Evaluate for Plasmodium parasites.
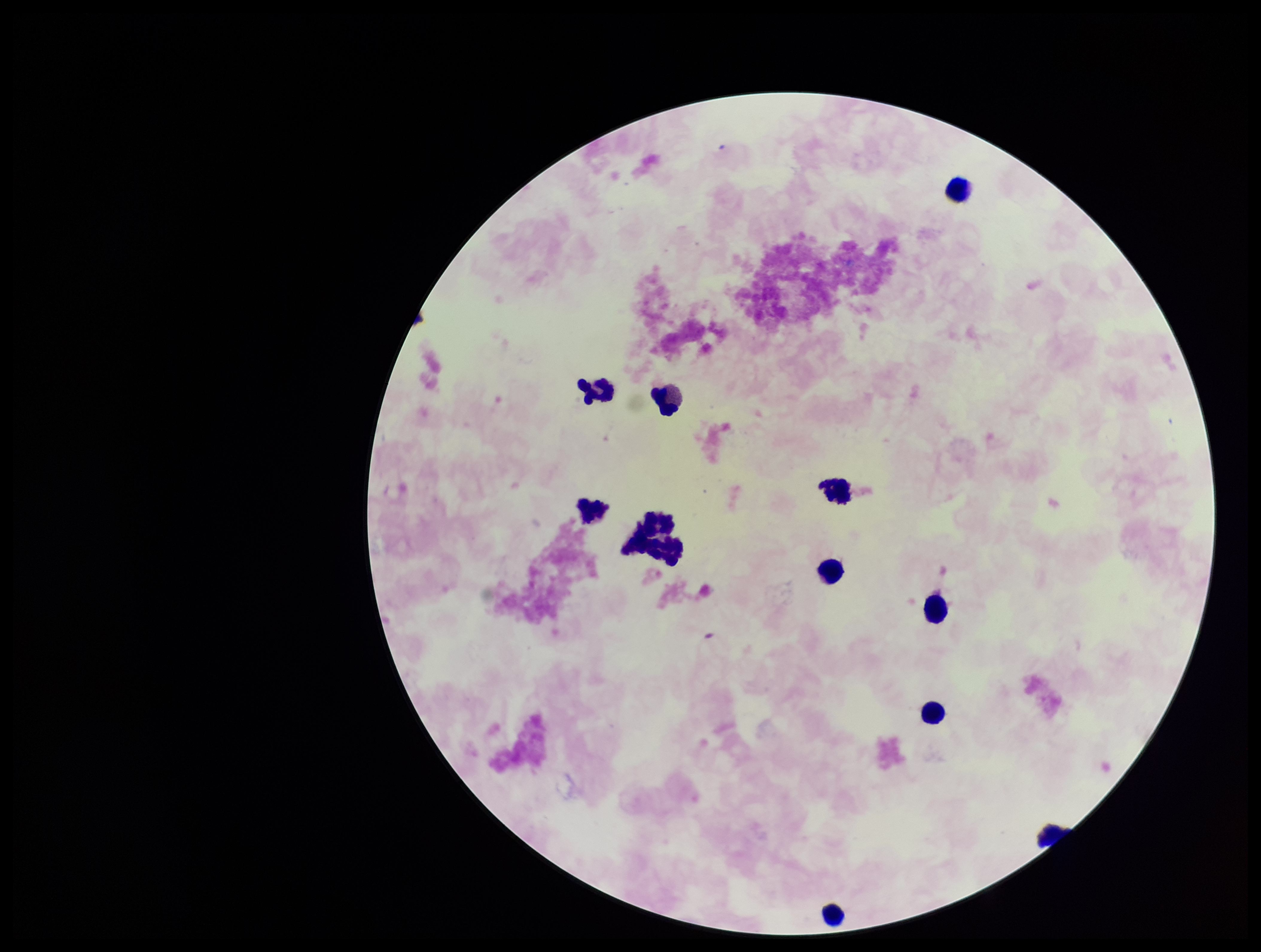

None detected.

Stained with Giemsa. Single field of view. Preparation: thick. Leukocyte count: 10. Parasite count: 0. Patient malaria status: negative. Smartphone photograph taken through the eyepiece of a microscope. Image is 1261×952 pixels.